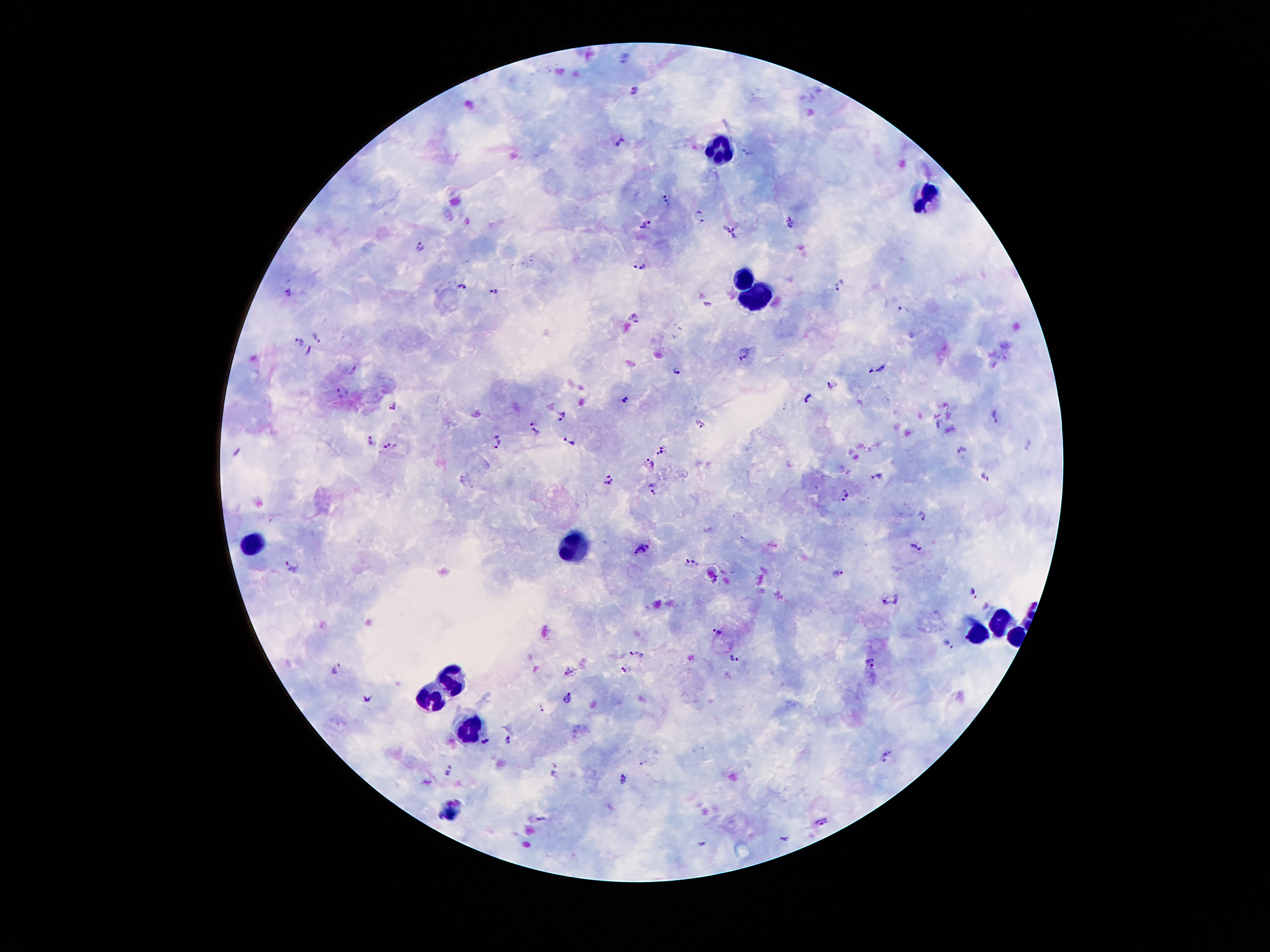

Approximate object centers, in pixels from the top-left corner.
Summary:
  - Plasmodium parasite locations: (x=623, y=59), (x=637, y=92), (x=619, y=142), (x=749, y=153), (x=666, y=200), (x=700, y=215), (x=791, y=222), (x=648, y=225), (x=724, y=226), (x=736, y=232), (x=420, y=247), (x=640, y=266), (x=839, y=285), (x=464, y=286), (x=287, y=292), (x=492, y=292), (x=708, y=305), (x=902, y=309), (x=634, y=321), (x=316, y=338), (x=301, y=342), (x=309, y=352), (x=744, y=357), (x=876, y=369), (x=354, y=370), (x=676, y=370), (x=831, y=387), (x=341, y=393), (x=808, y=398), (x=626, y=401), (x=393, y=406), (x=562, y=415), (x=995, y=417), (x=940, y=422), (x=701, y=424), (x=534, y=429), (x=370, y=440), (x=570, y=441), (x=498, y=443), (x=389, y=446), (x=659, y=451), (x=962, y=451), (x=648, y=463), (x=876, y=476), (x=986, y=476), (x=608, y=481), (x=653, y=489), (x=847, y=497), (x=922, y=516), (x=917, y=547), (x=642, y=549), (x=690, y=561), (x=292, y=566), (x=838, y=573), (x=715, y=581), (x=973, y=594), (x=891, y=599), (x=717, y=631), (x=947, y=644), (x=638, y=655), (x=733, y=659), (x=872, y=662), (x=335, y=668), (x=626, y=670), (x=572, y=671), (x=369, y=698), (x=568, y=699), (x=542, y=709), (x=484, y=740), (x=509, y=740), (x=886, y=756), (x=641, y=763), (x=448, y=769), (x=624, y=780), (x=542, y=818), (x=821, y=822), (x=784, y=839), (x=703, y=844)
  - Leukocyte locations: (x=715, y=148), (x=924, y=199), (x=747, y=274), (x=757, y=296), (x=254, y=542), (x=574, y=549), (x=1002, y=616), (x=978, y=631), (x=1016, y=636), (x=450, y=672), (x=436, y=697), (x=469, y=727)
  - Field of view: one from this slide
  - Capture: smartphone through the microscope eyepiece
  - Magnification: 100x
  - Image size: 1270×952 pixels
  - Stain: Giemsa
  - Patient malaria status: positive for Plasmodium falciparum
  - Preparation: thick peripheral-blood smear